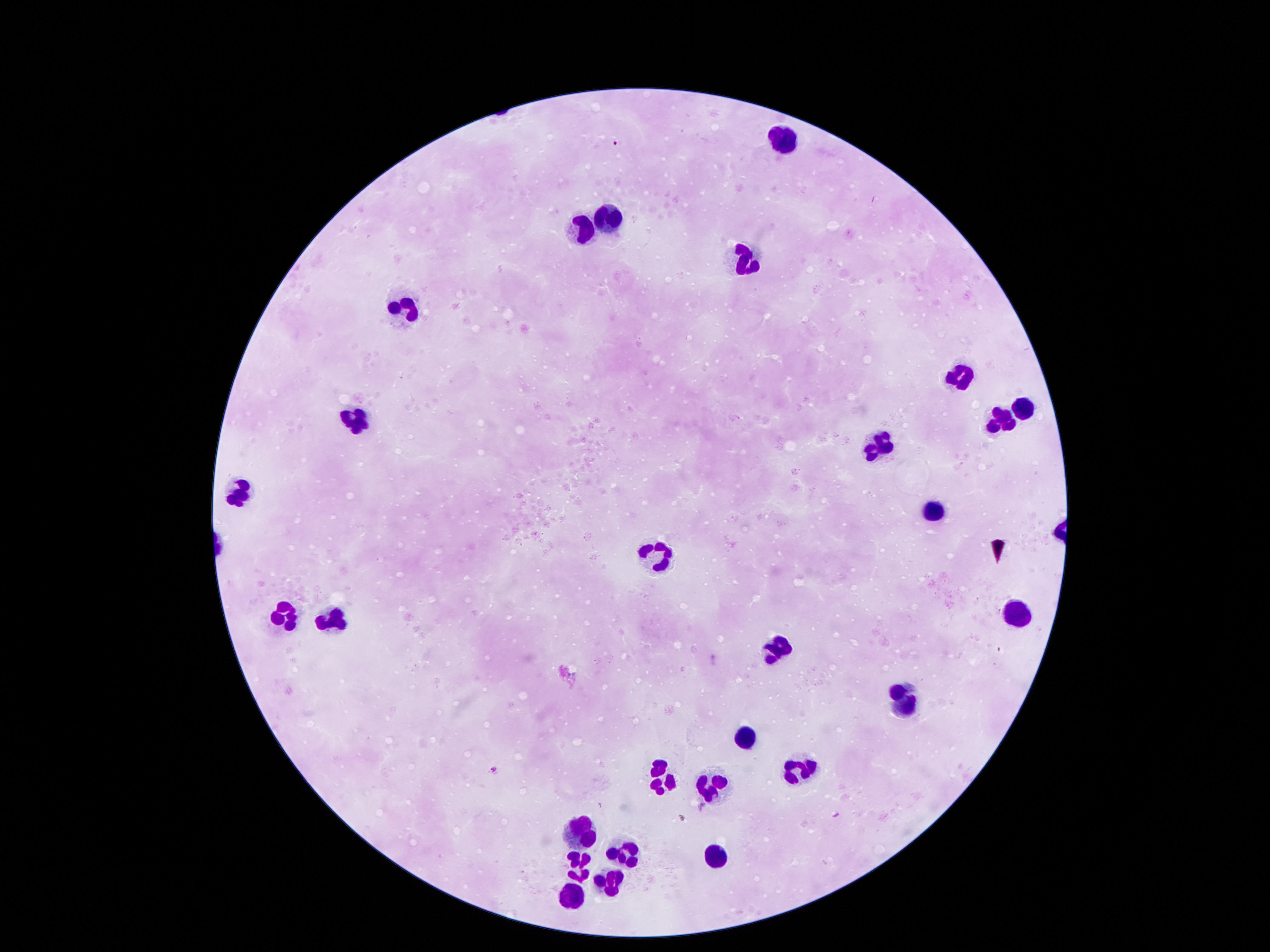
field_of_view: single
preparation: thick blood film
capture: smartphone camera through the microscope eyepiece
stain: Giemsa
leukocyte_locations: 'approximate object centers, in pixels from the top-left corner: (x=784, y=133), (x=605, y=215), (x=582, y=233), (x=742, y=256), (x=407, y=305), (x=954, y=379), (x=1020, y=407), (x=352, y=420), (x=998, y=420), (x=875, y=439), (x=242, y=482), (x=931, y=508), (x=658, y=548), (x=286, y=609), (x=1013, y=610), (x=328, y=618), (x=781, y=644), (x=901, y=701), (x=738, y=739), (x=666, y=770), (x=800, y=770), (x=711, y=786), (x=581, y=829), (x=622, y=853), (x=714, y=860), (x=581, y=863), (x=608, y=879), (x=570, y=891)'
magnification: 100x
image_size: 1270×952 pixels
patient_malaria_status: negative